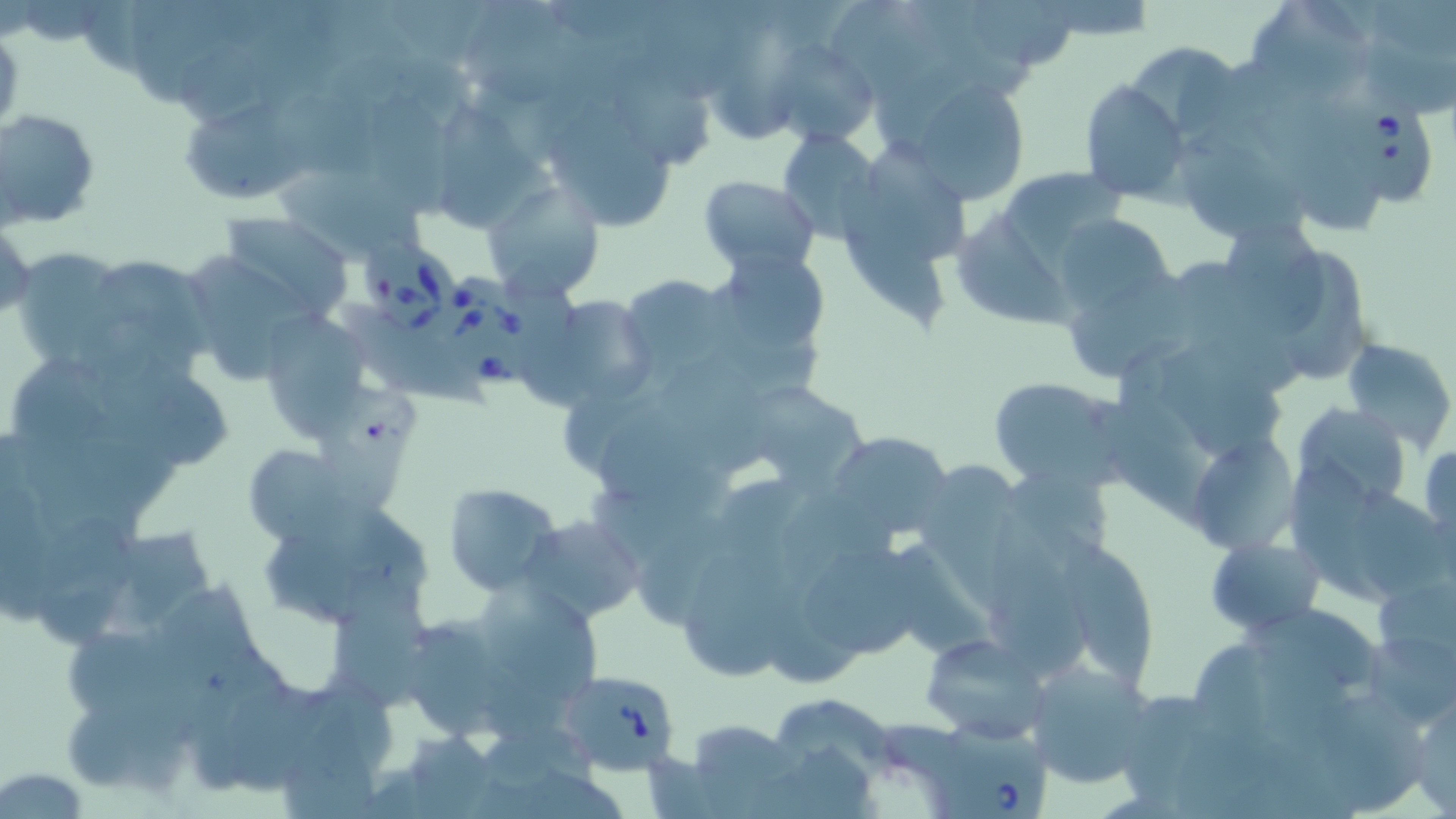
Summary:
  - Coordinate format: approximate bounding boxes as [x1, y1, x2, y2] in pixels
  - Uninfected red blood cell locations: [974, 0, 1076, 67], [1250, 0, 1371, 102], [124, 1, 226, 104], [464, 1, 572, 104], [837, 1, 943, 101], [770, 39, 879, 150], [1129, 41, 1243, 147], [612, 63, 711, 175], [904, 76, 1033, 205], [1080, 83, 1186, 200], [271, 88, 383, 179], [366, 94, 462, 219], [536, 95, 687, 234], [438, 98, 535, 230], [1261, 101, 1385, 238], [185, 103, 301, 202], [0, 108, 102, 229], [777, 127, 880, 241], [1178, 130, 1307, 235], [871, 139, 971, 258], [274, 168, 429, 257], [1009, 169, 1127, 271], [698, 176, 820, 273], [481, 180, 605, 303], [841, 180, 945, 333], [953, 199, 1079, 335], [1220, 210, 1323, 344], [218, 212, 356, 324], [1, 220, 36, 326], [1065, 220, 1172, 317], [12, 247, 131, 367], [1284, 248, 1373, 380], [711, 249, 832, 360], [74, 251, 221, 380], [175, 252, 320, 389], [1068, 272, 1197, 381], [617, 273, 741, 383], [538, 292, 655, 407], [259, 308, 378, 444], [1343, 338, 1455, 449], [1160, 347, 1284, 469], [94, 363, 233, 467], [989, 376, 1126, 490], [740, 380, 874, 496], [1100, 381, 1220, 530], [1292, 403, 1411, 515], [607, 416, 747, 517], [828, 430, 955, 541], [1195, 440, 1303, 554], [1420, 443, 1455, 546], [242, 445, 359, 546], [921, 460, 1027, 608], [1293, 460, 1390, 606], [444, 483, 563, 596], [1362, 489, 1456, 602], [45, 515, 141, 654], [518, 515, 644, 624], [986, 518, 1099, 675], [1058, 523, 1157, 690], [265, 527, 384, 629], [1206, 536, 1322, 635], [806, 546, 945, 657], [678, 553, 793, 686], [333, 567, 433, 705], [159, 575, 271, 747], [481, 586, 602, 704], [1242, 606, 1387, 691], [404, 616, 517, 739], [66, 631, 178, 712], [922, 632, 1047, 742], [1366, 637, 1456, 721], [1023, 661, 1154, 788], [67, 690, 146, 787], [1314, 692, 1427, 813], [1409, 693, 1456, 815], [775, 697, 901, 789], [1124, 697, 1216, 814], [280, 704, 382, 819], [683, 719, 801, 816], [397, 731, 503, 818], [0, 766, 91, 816]
  - Babesia divergens-infected red blood cell locations: [1337, 92, 1434, 210], [360, 239, 459, 331], [446, 272, 546, 393], [560, 666, 677, 780], [923, 716, 1052, 819]
  - Slide-level diagnosis: Babesia divergens
  - Modality: optical microscopy
  - Stain: May-Grünwald-Giemsa
  - Field of view: single
  - Image size: 1456×819 pixels
  - Preparation: thin blood film
  - Magnification: 1000x